Assess this cell for malaria.
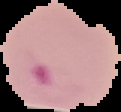

Parasitized.

Summary:
  - Image type: segmented cell region on a black background
  - Image size: 121×112 pixels
  - Preparation: thin blood film